Evaluate for malaria.
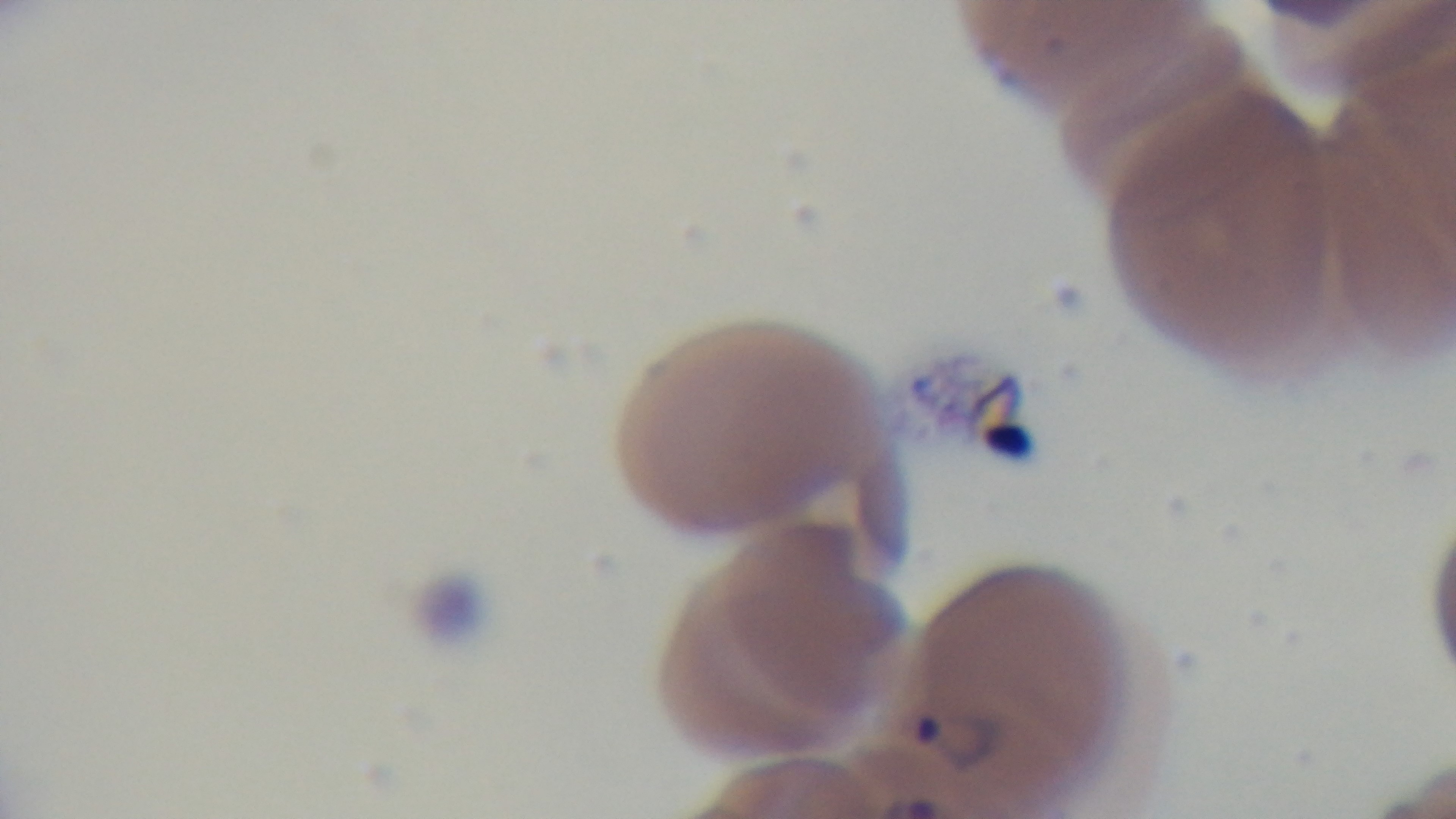

Infected.

modality = light microscopy
capture = mounted 4K digital camera
stain = Giemsa
objective = 100x oil immersion
field of view = one from the slide
preparation = thin